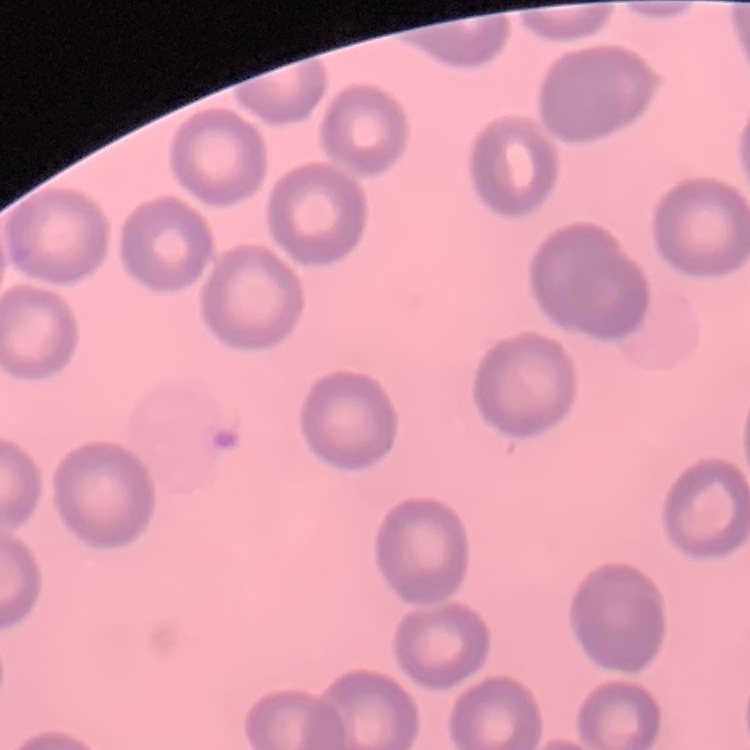

The red blood cells exhibit no rouleaux formation. Field's or Giemsa stain. Thin peripheral smear. One tile cut from a larger photomicrograph.